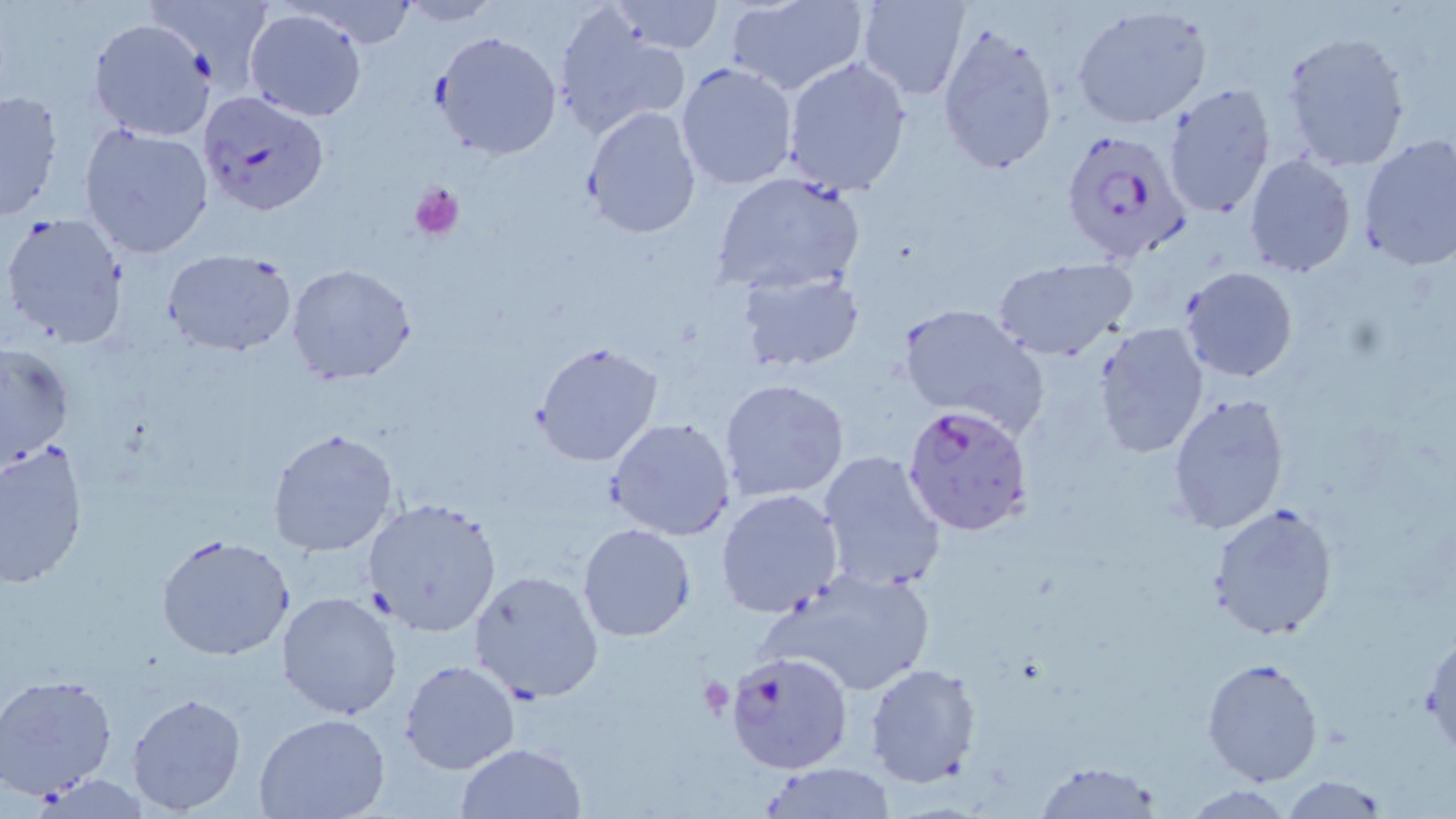 Approximate bounding boxes as named x1/y1/x2/y2 corners in pixels. Platelet locations: (x1=407, y1=181, x2=465, y2=243), (x1=698, y1=676, x2=734, y2=719). Uninfected red blood cell locations: (x1=144, y1=0, x2=277, y2=81), (x1=607, y1=0, x2=727, y2=54), (x1=722, y1=0, x2=869, y2=97), (x1=855, y1=0, x2=971, y2=100), (x1=298, y1=1, x2=417, y2=46), (x1=394, y1=1, x2=500, y2=26), (x1=1072, y1=4, x2=1211, y2=128), (x1=553, y1=7, x2=690, y2=140), (x1=244, y1=8, x2=367, y2=122), (x1=89, y1=19, x2=213, y2=139), (x1=936, y1=22, x2=1059, y2=175), (x1=432, y1=30, x2=560, y2=159), (x1=1280, y1=30, x2=1412, y2=173), (x1=781, y1=55, x2=912, y2=194), (x1=676, y1=62, x2=798, y2=189), (x1=1161, y1=85, x2=1277, y2=216), (x1=0, y1=88, x2=64, y2=224), (x1=580, y1=105, x2=702, y2=239), (x1=78, y1=124, x2=213, y2=259), (x1=1357, y1=135, x2=1456, y2=270), (x1=1243, y1=153, x2=1356, y2=278), (x1=711, y1=172, x2=867, y2=297), (x1=1, y1=212, x2=127, y2=350), (x1=161, y1=248, x2=297, y2=355), (x1=992, y1=256, x2=1139, y2=362), (x1=285, y1=263, x2=417, y2=385), (x1=1179, y1=266, x2=1297, y2=382), (x1=736, y1=268, x2=865, y2=373), (x1=895, y1=302, x2=1050, y2=436), (x1=1093, y1=323, x2=1209, y2=459), (x1=533, y1=340, x2=664, y2=467), (x1=1, y1=341, x2=75, y2=473), (x1=719, y1=376, x2=852, y2=502), (x1=1167, y1=392, x2=1291, y2=534), (x1=606, y1=416, x2=737, y2=541), (x1=267, y1=427, x2=401, y2=557), (x1=0, y1=439, x2=89, y2=590), (x1=816, y1=450, x2=949, y2=594), (x1=715, y1=489, x2=845, y2=618), (x1=361, y1=495, x2=503, y2=637), (x1=1205, y1=502, x2=1339, y2=642), (x1=577, y1=523, x2=698, y2=642), (x1=153, y1=533, x2=299, y2=662), (x1=762, y1=564, x2=938, y2=697), (x1=468, y1=568, x2=603, y2=703), (x1=276, y1=591, x2=404, y2=720), (x1=1422, y1=627, x2=1455, y2=758), (x1=1201, y1=657, x2=1325, y2=787), (x1=398, y1=659, x2=520, y2=775), (x1=864, y1=663, x2=982, y2=788), (x1=1, y1=674, x2=119, y2=799), (x1=126, y1=691, x2=248, y2=815), (x1=253, y1=713, x2=390, y2=819), (x1=454, y1=741, x2=584, y2=818), (x1=1032, y1=759, x2=1167, y2=817), (x1=753, y1=762, x2=901, y2=817), (x1=25, y1=773, x2=158, y2=817), (x1=1279, y1=775, x2=1392, y2=817). Plasmodium falciparum-infected red blood cell locations: (x1=199, y1=91, x2=330, y2=218), (x1=1061, y1=129, x2=1192, y2=268), (x1=901, y1=402, x2=1035, y2=537), (x1=725, y1=648, x2=851, y2=774). Slide-level diagnosis: Plasmodium falciparum. Single field of view. Image is 1456×819 pixels. Light microscopy. May-Grünwald-Giemsa-stained preparation. 1000x magnification. Thin blood film.